Assess this cell for malaria.
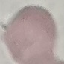

Uninfected.

{
  "image_type": "automatically extracted cell patch, resized to 64 × 64 pixels",
  "stain": "Giemsa",
  "capture": "smartphone camera at the microscope eyepiece",
  "preparation": "thin smear"
}